Give the extent of all uninfected red blood cells.
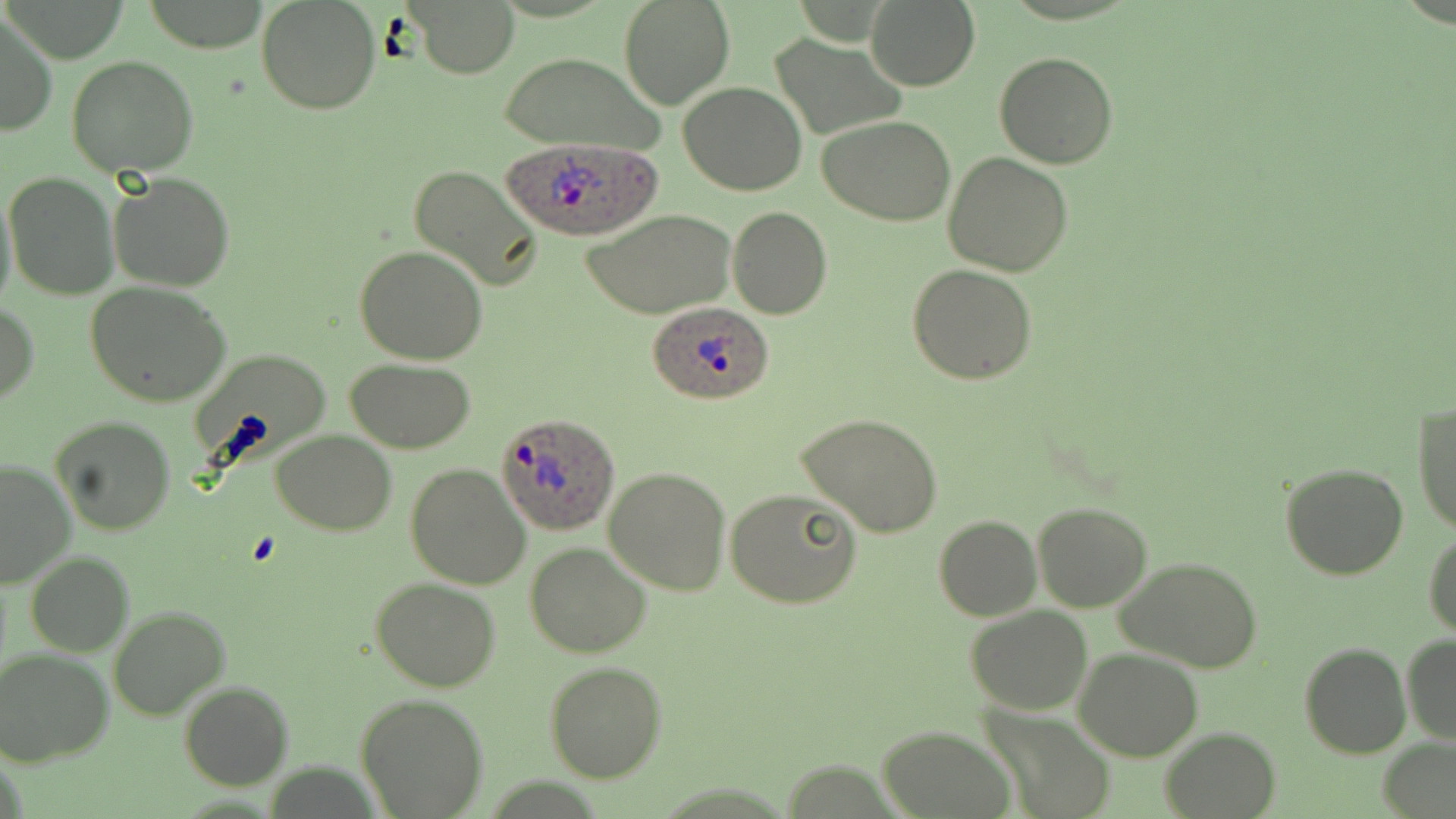

Approximate bounding boxes as (x1, y1, x2, y2) in pixels.
Uninfected red blood cells: (257, 0, 382, 116), (618, 0, 737, 111), (865, 0, 980, 91), (412, 1, 519, 77), (1, 12, 56, 138), (770, 32, 907, 141), (501, 52, 663, 156), (994, 53, 1119, 169), (66, 55, 199, 178), (679, 82, 808, 196), (818, 116, 956, 226), (944, 153, 1073, 276), (407, 163, 543, 293), (5, 171, 118, 299), (107, 172, 236, 293), (0, 186, 17, 315), (726, 207, 832, 319), (583, 210, 736, 319), (354, 245, 489, 365), (907, 264, 1037, 385), (84, 282, 232, 407), (0, 301, 38, 408), (346, 359, 477, 452), (1411, 400, 1456, 536), (797, 414, 946, 539), (49, 416, 177, 537), (272, 431, 397, 534), (0, 458, 77, 591), (1278, 462, 1410, 582), (405, 464, 531, 589), (604, 465, 731, 596), (726, 489, 864, 609), (1032, 501, 1153, 613), (934, 515, 1041, 621), (1425, 529, 1456, 637), (525, 543, 653, 658), (25, 551, 132, 657), (1117, 558, 1262, 673), (371, 578, 502, 693), (108, 605, 231, 719), (964, 605, 1095, 714), (1401, 634, 1456, 744), (1299, 642, 1410, 758), (1, 648, 117, 769), (1075, 648, 1205, 762), (544, 661, 667, 783), (178, 681, 293, 791), (355, 693, 489, 817), (979, 708, 1114, 819), (879, 725, 1016, 818), (1160, 726, 1280, 818), (1376, 738, 1455, 819).

Summary:
  - Plasmodium ovale-infected red blood cell locations: (500, 138, 662, 240), (648, 300, 776, 406), (496, 411, 619, 533)
  - Slide-level diagnosis: Plasmodium ovale
  - Stain: May-Grünwald-Giemsa
  - Field of view: single
  - Magnification: 1000x
  - Modality: light microscopy
  - Image size: 1456×819 pixels
  - Preparation: thin blood smear